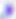

modality: photomicrograph
magnification: 400x
identification: Toxoplasma gondii